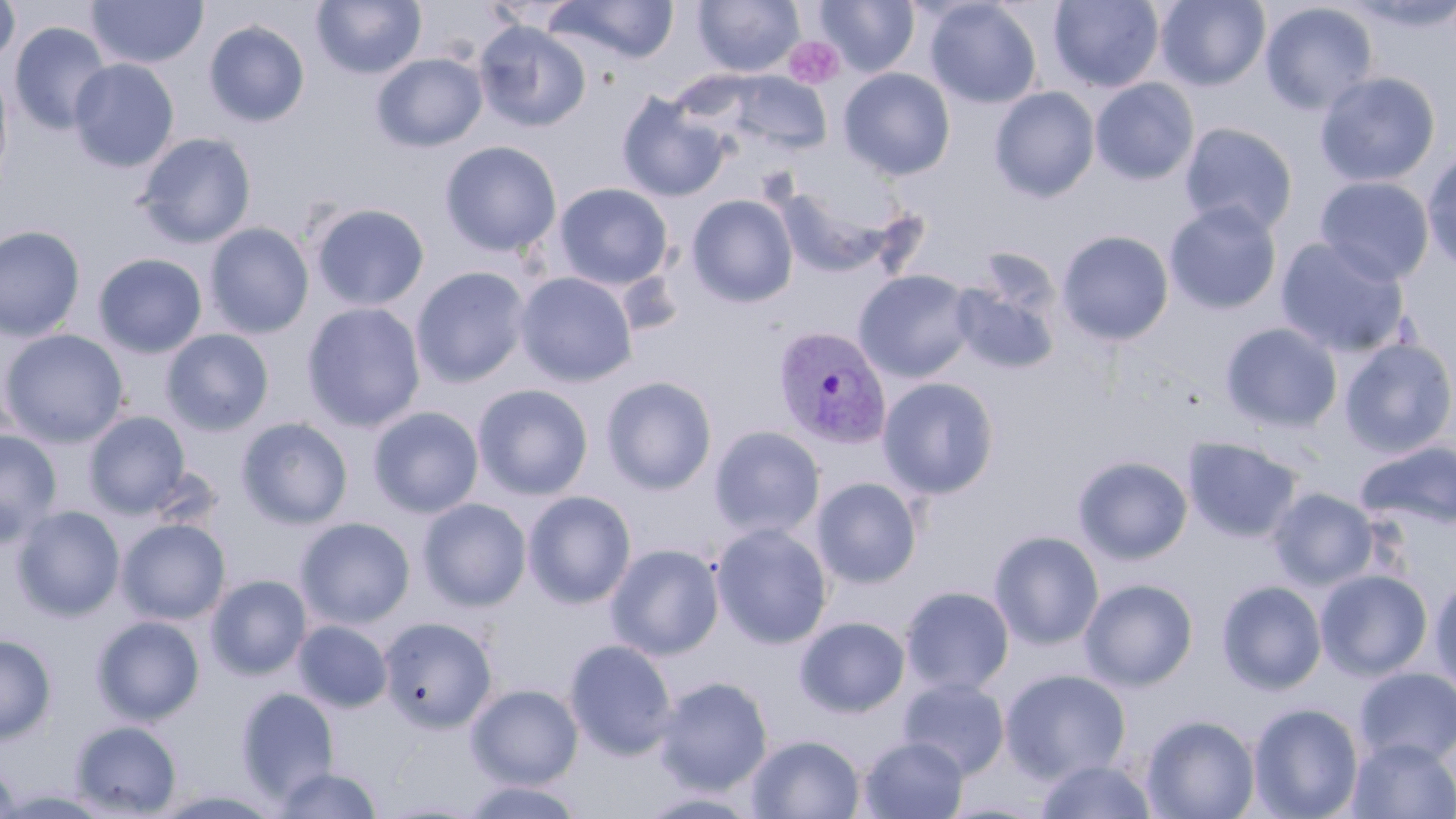
slide-level diagnosis = Plasmodium vivax
modality = light microscopy
platelet locations = approximate bounding boxes as (x1,y1)-(x2,y2) corner pairs in pixels: (784,37)-(845,89)
field of view = single
magnification = 1000x
preparation = thin blood film
Plasmodium vivax-infected red blood cell locations = approximate bounding boxes as (x1,y1)-(x2,y2) corner pairs in pixels: (773,326)-(892,450)
uninfected red blood cell locations = approximate bounding boxes as (x1,y1)-(x2,y2) corner pairs in pixels: (86,0)-(208,69), (311,0)-(427,79), (693,0)-(804,77), (815,0)-(919,77), (924,0)-(1042,109), (1049,0)-(1164,92), (1155,0)-(1270,90), (0,1)-(20,67), (548,1)-(680,63), (1259,2)-(1378,116), (204,20)-(310,127), (474,20)-(591,133), (10,22)-(112,135), (371,52)-(488,152), (69,59)-(179,172), (0,63)-(14,195), (838,68)-(956,181), (723,72)-(833,154), (1315,72)-(1441,187), (1091,78)-(1199,185), (989,86)-(1100,202), (616,91)-(729,202), (1179,122)-(1298,236), (136,133)-(256,248), (439,141)-(563,256), (1422,149)-(1456,273), (1315,176)-(1434,285), (553,183)-(673,289), (774,183)-(901,278), (687,194)-(798,307), (1164,201)-(1283,315), (309,202)-(430,311), (204,223)-(314,338), (0,225)-(85,342), (1057,230)-(1174,346), (1275,238)-(1410,358), (93,253)-(207,358), (411,266)-(530,388), (854,269)-(976,382), (514,271)-(638,387), (951,279)-(1059,375), (302,302)-(426,433), (1220,322)-(1343,434), (1,329)-(128,447), (161,329)-(275,436), (1221,330)-(1455,448), (1339,338)-(1456,458), (601,376)-(717,495), (878,376)-(1000,499), (472,384)-(594,500), (368,406)-(484,518), (84,411)-(190,518), (236,417)-(353,529), (709,425)-(825,539), (0,429)-(62,546), (1183,437)-(1303,542), (1356,440)-(1456,530), (1073,455)-(1194,565), (811,477)-(923,588), (1268,488)-(1379,590), (523,490)-(636,608), (418,497)-(532,611), (12,505)-(125,621), (296,517)-(415,628), (117,519)-(230,624), (711,522)-(833,649), (989,530)-(1104,650), (606,543)-(724,660), (1316,569)-(1433,680), (205,574)-(312,679), (1430,575)-(1456,697), (1080,578)-(1198,690), (1217,580)-(1327,694), (901,586)-(1014,695), (91,615)-(205,725), (379,616)-(498,733), (795,616)-(910,717), (293,620)-(392,713), (0,634)-(57,744), (564,639)-(678,759), (1354,667)-(1456,767), (1001,668)-(1132,783), (654,676)-(772,794), (898,677)-(1010,779), (467,684)-(583,789), (236,687)-(340,803), (1249,703)-(1363,819), (1142,714)-(1260,819), (70,720)-(182,817), (746,734)-(865,818), (858,735)-(969,819), (1347,737)-(1456,818), (1035,758)-(1159,819), (0,759)-(20,819), (272,766)-(384,818), (460,779)-(585,819), (0,787)-(114,818), (151,788)-(288,818), (635,789)-(765,818)
stain = May-Grünwald-Giemsa
image size = 1456×819 pixels